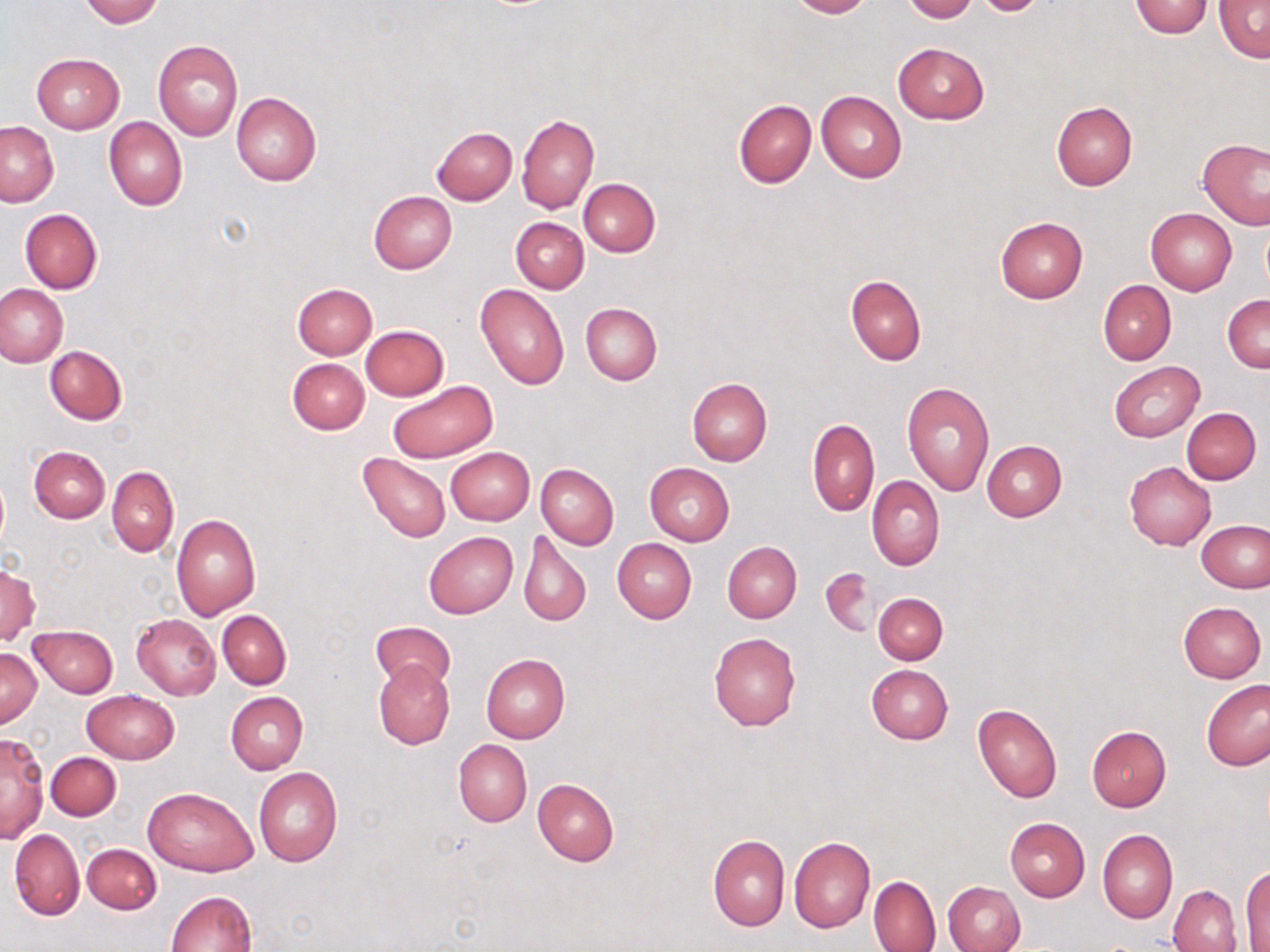
slide-level diagnosis = negative for blood parasites
uninfected red blood cell locations = approximate bounding boxes as named x1/y1/x2/y2 corners in pixels: (x1=79, y1=0, x2=164, y2=26), (x1=787, y1=0, x2=872, y2=18), (x1=902, y1=0, x2=978, y2=22), (x1=1214, y1=0, x2=1270, y2=64), (x1=1128, y1=2, x2=1214, y2=38), (x1=154, y1=40, x2=243, y2=140), (x1=893, y1=43, x2=989, y2=123), (x1=32, y1=53, x2=124, y2=133), (x1=816, y1=90, x2=907, y2=182), (x1=231, y1=91, x2=322, y2=186), (x1=733, y1=99, x2=816, y2=188), (x1=1051, y1=101, x2=1138, y2=189), (x1=517, y1=113, x2=599, y2=213), (x1=104, y1=116, x2=187, y2=211), (x1=0, y1=121, x2=59, y2=208), (x1=432, y1=127, x2=517, y2=204), (x1=1197, y1=138, x2=1269, y2=230), (x1=578, y1=178, x2=660, y2=256), (x1=368, y1=191, x2=457, y2=274), (x1=20, y1=208, x2=102, y2=293), (x1=1146, y1=208, x2=1237, y2=294), (x1=995, y1=216, x2=1089, y2=302), (x1=511, y1=217, x2=588, y2=292), (x1=844, y1=274, x2=925, y2=366), (x1=1099, y1=279, x2=1176, y2=365), (x1=292, y1=282, x2=377, y2=358), (x1=475, y1=283, x2=570, y2=390), (x1=0, y1=284, x2=68, y2=366), (x1=1223, y1=295, x2=1270, y2=372), (x1=580, y1=303, x2=662, y2=385), (x1=361, y1=325, x2=449, y2=400), (x1=44, y1=345, x2=126, y2=425), (x1=287, y1=357, x2=370, y2=434), (x1=1108, y1=361, x2=1204, y2=442), (x1=687, y1=378, x2=772, y2=466), (x1=387, y1=380, x2=497, y2=464), (x1=902, y1=382, x2=995, y2=497), (x1=1182, y1=407, x2=1261, y2=484), (x1=807, y1=417, x2=880, y2=517), (x1=981, y1=439, x2=1067, y2=521), (x1=29, y1=445, x2=109, y2=522), (x1=445, y1=447, x2=534, y2=526), (x1=358, y1=452, x2=451, y2=542), (x1=644, y1=462, x2=735, y2=545), (x1=1124, y1=462, x2=1216, y2=549), (x1=536, y1=463, x2=619, y2=549), (x1=107, y1=465, x2=179, y2=557), (x1=866, y1=476, x2=944, y2=571), (x1=171, y1=513, x2=261, y2=619), (x1=1198, y1=521, x2=1270, y2=592), (x1=519, y1=530, x2=591, y2=626), (x1=424, y1=531, x2=519, y2=619), (x1=613, y1=538, x2=696, y2=623), (x1=722, y1=542, x2=802, y2=622), (x1=0, y1=566, x2=39, y2=645), (x1=821, y1=567, x2=879, y2=637), (x1=872, y1=592, x2=949, y2=665), (x1=1177, y1=601, x2=1266, y2=683), (x1=218, y1=609, x2=290, y2=689), (x1=132, y1=614, x2=221, y2=699), (x1=371, y1=620, x2=456, y2=691), (x1=28, y1=625, x2=118, y2=697), (x1=709, y1=633, x2=802, y2=731), (x1=1, y1=649, x2=41, y2=727), (x1=481, y1=653, x2=571, y2=742), (x1=373, y1=660, x2=454, y2=749), (x1=865, y1=663, x2=953, y2=745), (x1=1201, y1=679, x2=1269, y2=771), (x1=83, y1=690, x2=179, y2=764), (x1=226, y1=691, x2=307, y2=774), (x1=973, y1=703, x2=1062, y2=803), (x1=1086, y1=725, x2=1171, y2=811), (x1=1, y1=732, x2=48, y2=845), (x1=453, y1=740, x2=532, y2=826), (x1=45, y1=751, x2=121, y2=821), (x1=254, y1=768, x2=342, y2=866), (x1=532, y1=778, x2=619, y2=865), (x1=144, y1=785, x2=255, y2=876), (x1=1003, y1=817, x2=1090, y2=902), (x1=9, y1=829, x2=84, y2=920), (x1=1098, y1=830, x2=1177, y2=924), (x1=708, y1=836, x2=790, y2=931), (x1=789, y1=837, x2=875, y2=932), (x1=82, y1=843, x2=162, y2=914), (x1=1241, y1=865, x2=1270, y2=951), (x1=868, y1=876, x2=942, y2=952), (x1=943, y1=880, x2=1025, y2=952), (x1=1168, y1=885, x2=1242, y2=952), (x1=168, y1=891, x2=257, y2=952)
preparation = thin blood smear
stain = May-Grünwald-Giemsa
field of view = single
modality = light microscopy
magnification = 1000x
image size = 1270×952 pixels